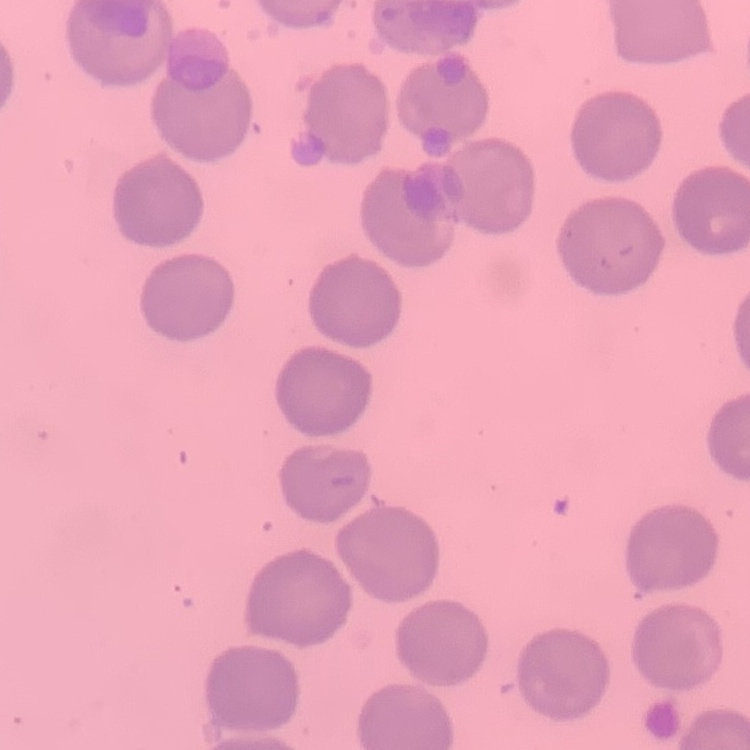
The erythrocytes show no rouleaux formation. Field's or Giemsa stain. Thin blood smear. Square crop of a larger photomicrograph.